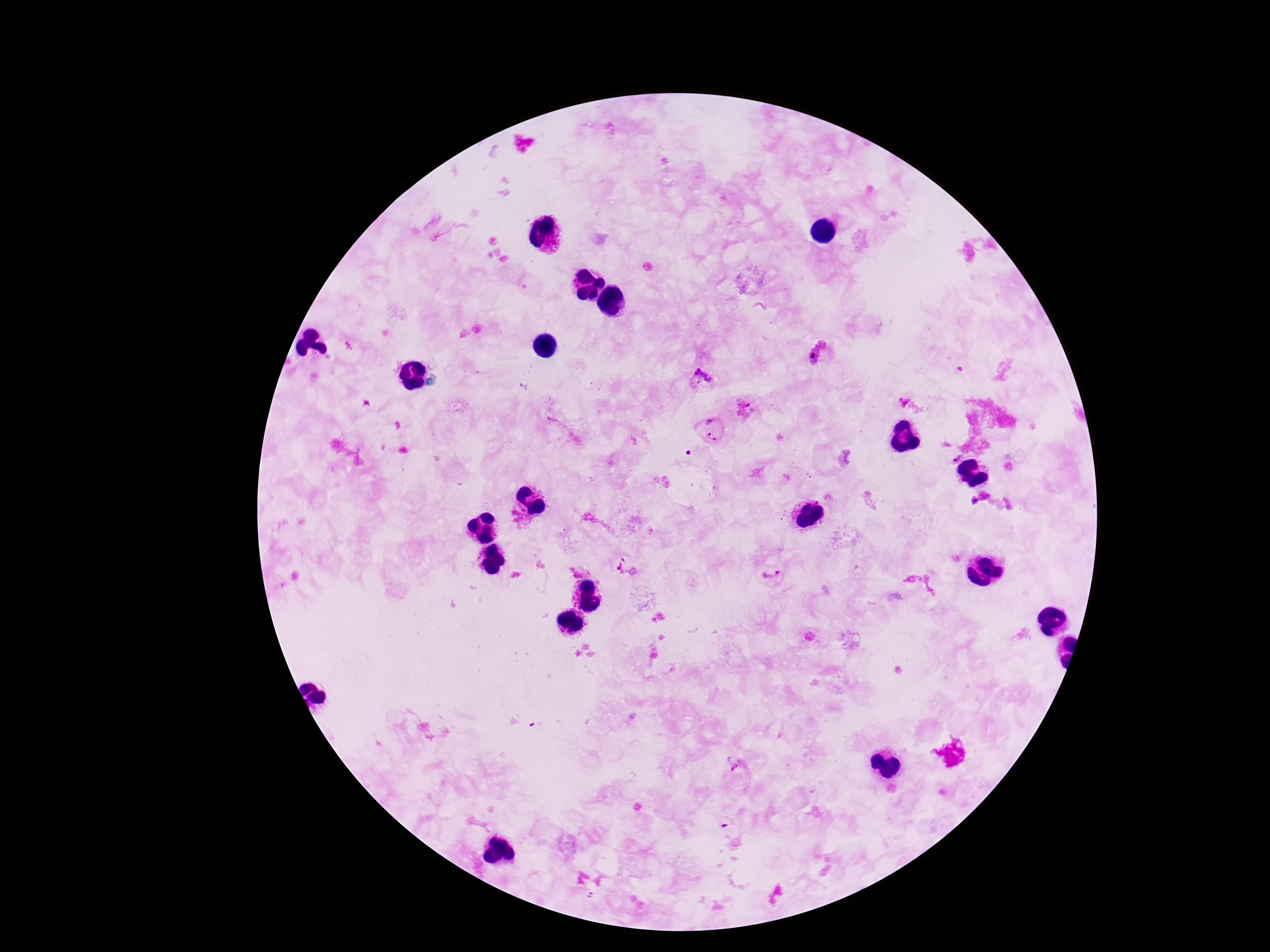

Approximate centers as {x, y} in pixels.
Summary:
  - Plasmodium parasite locations: {817, 353}, {703, 380}, {744, 410}, {713, 429}, {809, 477}, {770, 574}, {736, 767}
  - Field of view: single
  - Magnification: 100x
  - Patient malaria status: infected
  - Capture: smartphone camera through the microscope eyepiece
  - Stain: Giemsa
  - Preparation: thick blood smear
  - Image size: 1270×952 pixels